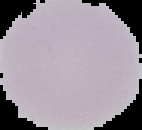

image size = 142×130 pixels
image type = cell region segmented out of the field of view; surrounding area masked to black
preparation = thin blood film
malaria status = uninfected